Name the cell type shown.
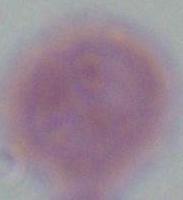
An erythrocyte.

Summary:
  - Modality: micrograph
  - Magnification: 1000x